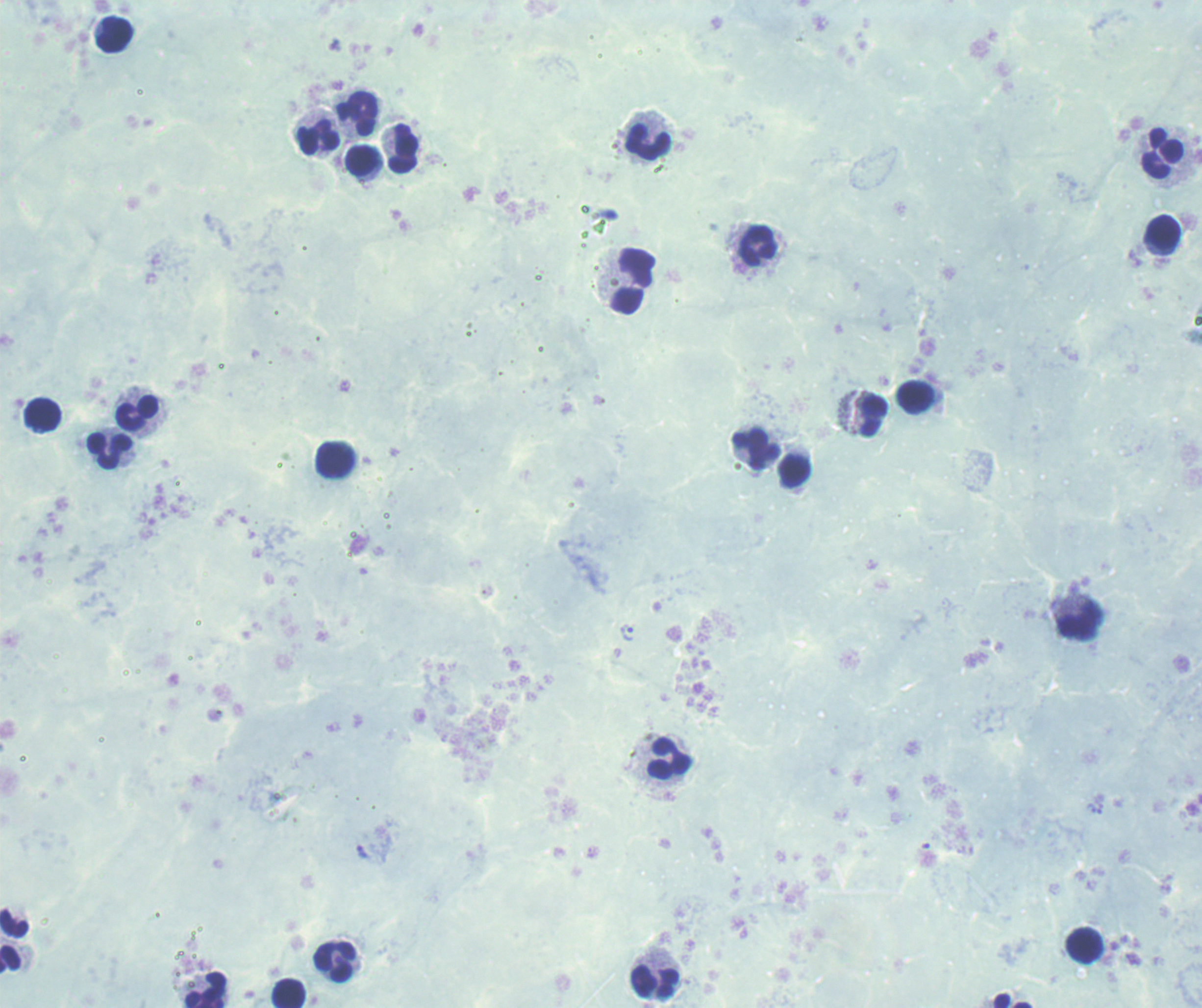

Approximate object centers, in pixels from the top-left corner.
Summary:
  - Trophozoite locations: (x=627, y=633)
  - Leukocyte locations: (x=115, y=35), (x=357, y=114), (x=319, y=137), (x=648, y=142), (x=403, y=149), (x=1163, y=153), (x=362, y=160), (x=1163, y=232), (x=759, y=245), (x=633, y=281), (x=916, y=396), (x=137, y=413), (x=43, y=414), (x=873, y=416), (x=757, y=449), (x=109, y=451), (x=335, y=461), (x=795, y=471), (x=1079, y=621), (x=669, y=758), (x=1085, y=947), (x=10, y=960), (x=335, y=961), (x=656, y=982), (x=206, y=990), (x=289, y=994), (x=1013, y=1000)
  - Background quality: poor
  - Magnification: 100x
  - Stain: Romanowsky
  - Image size: 1202×1008 pixels
  - Context: previously used in a real diagnosis
  - Result: Plasmodium parasites identified
  - Preparation: thick blood film
  - Field of view: single